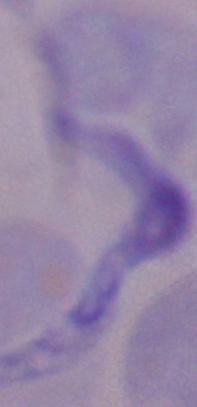
modality = micrograph
identification = trypanosome
magnification = 1000x